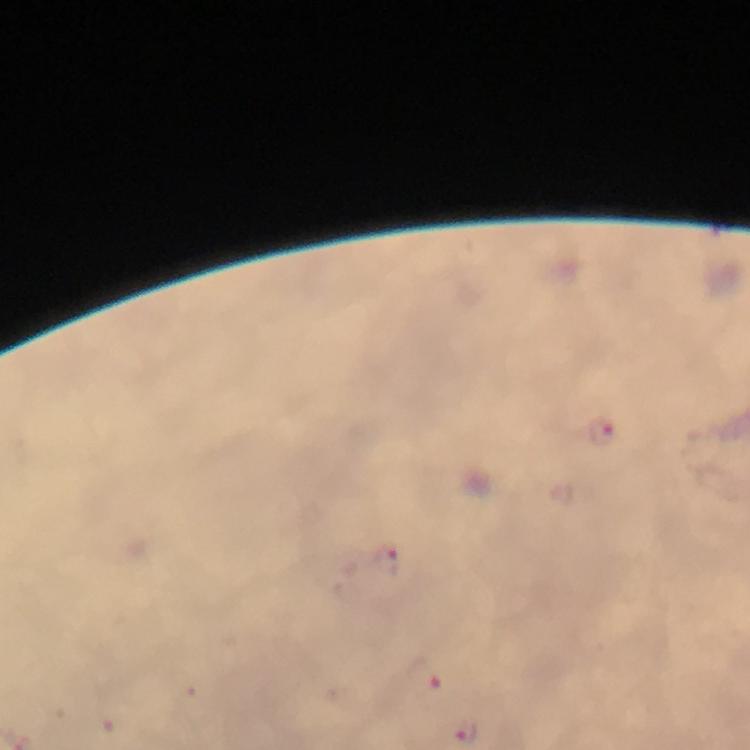
magnification = 100x
immersion oil = used
image size = 750×750 pixels
malaria parasite locations = approximate centers as [x, y] in pixels: [599, 431], [388, 558], [422, 677]
capture = smartphone mounted on the microscope
preparation = thick blood smear
cropped from = a single field of view
stain = Giemsa
context = from a malaria diagnostic workup